Report the malaria status of this cell.
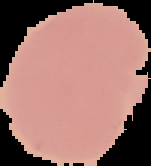

It is uninfected.

Summary:
  - Image type: segmented cell region with the area outside set to black
  - Image size: 151×166 pixels
  - Preparation: thin blood film